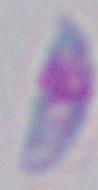

Micrograph. 1000x magnification. Toxoplasma gondii is seen.